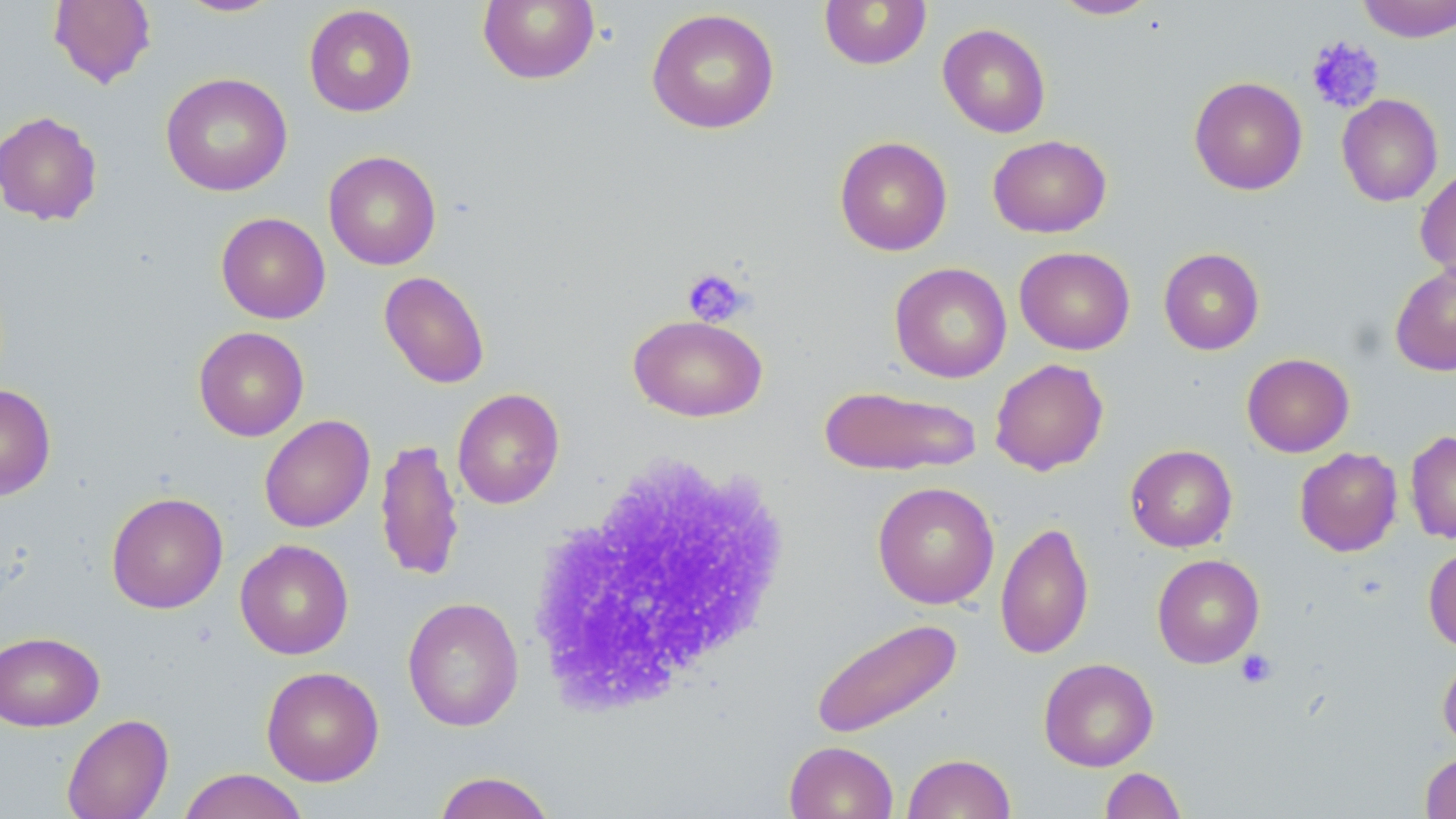

slide_level_diagnosis: negative for blood parasites
stain: May-Grünwald-Giemsa
preparation: thin blood film
platelet_locations: 'approximate bounding boxes as (x1,y1)-(x2,y2) corner pairs in pixels: (1305,35)-(1385,113), (683,267)-(753,328), (1235,649)-(1277,688)'
modality: light microscopy
magnification: 1000x
uninfected_red_blood_cell_locations: 'approximate bounding boxes as (x1,y1)-(x2,y2) corner pairs in pixels: (48,0)-(156,88), (174,0)-(284,18), (478,0)-(600,85), (819,0)-(932,70), (1051,0)-(1159,19), (1357,0)-(1456,43), (303,4)-(418,117), (646,7)-(780,134), (937,23)-(1051,138), (160,72)-(292,197), (1189,76)-(1308,195), (1336,94)-(1443,207), (0,110)-(103,227), (988,134)-(1111,238), (834,136)-(953,256), (323,150)-(441,270), (1415,166)-(1456,283), (216,212)-(330,323), (1014,246)-(1135,355), (1158,248)-(1265,355), (889,262)-(1012,383), (1389,262)-(1456,377), (379,271)-(490,389), (628,315)-(767,421), (193,326)-(309,441), (1241,353)-(1355,457), (990,358)-(1109,476), (0,383)-(56,500), (818,384)-(982,476), (452,388)-(564,509), (259,414)-(375,533), (1405,430)-(1456,544), (375,437)-(465,583), (1125,444)-(1238,552), (1294,447)-(1402,556), (872,481)-(1000,609), (106,491)-(228,614), (995,520)-(1094,660), (235,539)-(354,660), (1423,546)-(1456,651), (1152,554)-(1265,668), (402,596)-(524,732), (810,617)-(963,739), (0,631)-(104,732), (1438,652)-(1456,753), (1038,657)-(1158,771), (261,666)-(384,786), (61,713)-(174,819), (784,741)-(898,819), (1420,751)-(1456,818), (903,753)-(1016,819), (1100,767)-(1186,819), (177,768)-(309,819), (433,770)-(557,819)'
image_size: 1456×819 pixels
white_blood_cell_locations: 'approximate bounding boxes as (x1,y1)-(x2,y2) corner pairs in pixels: (527,447)-(798,714)'
field_of_view: one of a larger specimen